Give the extent of all Plasmodium falciparum-infected red blood cells.
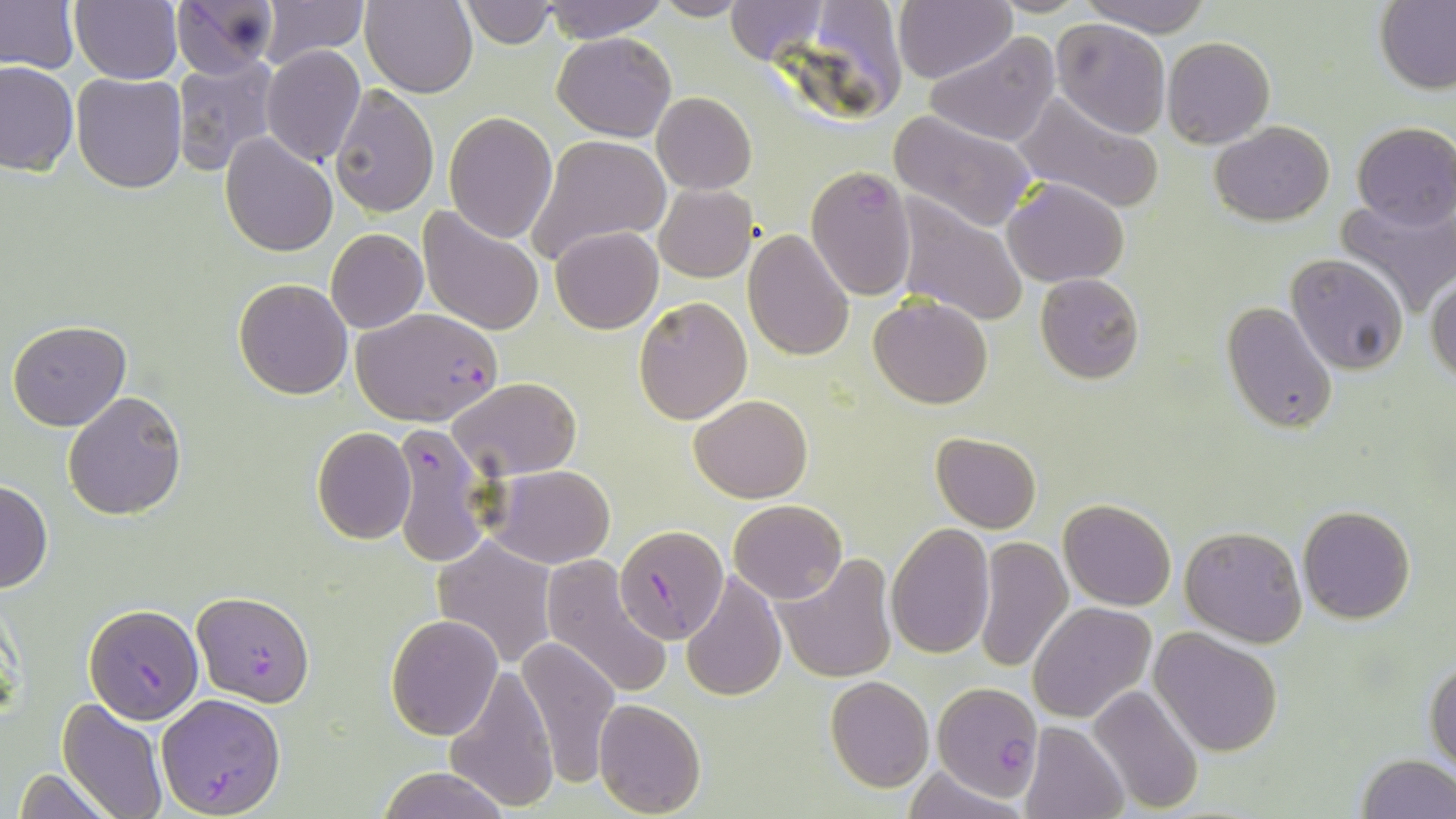

Approximate bounding boxes as (x1,y1)-(x2,y2) corner pairs in pixels.
Plasmodium falciparum-infected red blood cells: (806,166)-(916,300), (352,309)-(504,426), (387,422)-(495,565), (613,523)-(726,643), (192,592)-(315,706), (83,604)-(205,723), (933,683)-(1042,801), (155,693)-(286,817).

Uninfected red blood cell locations: (0,0)-(80,74), (173,0)-(276,78), (360,0)-(477,96), (460,0)-(558,48), (538,0)-(671,44), (651,0)-(753,21), (724,0)-(830,65), (893,0)-(1013,85), (1081,0)-(1213,37), (69,1)-(183,84), (257,1)-(367,66), (1376,2)-(1456,94), (1052,18)-(1170,138), (552,30)-(676,141), (922,31)-(1061,147), (1162,37)-(1275,149), (261,44)-(366,167), (171,55)-(279,175), (1,60)-(78,175), (188,66)-(308,225), (71,73)-(189,193), (330,85)-(438,218), (1011,87)-(1164,214), (652,92)-(756,193), (443,112)-(558,243), (889,112)-(1037,233), (1209,120)-(1336,226), (1351,120)-(1456,230), (220,133)-(338,258), (525,133)-(671,267), (1003,178)-(1129,288), (654,184)-(756,282), (892,193)-(1030,328), (1333,193)-(1456,318), (418,209)-(544,335), (550,226)-(663,334), (742,227)-(855,361), (326,229)-(427,333), (1284,254)-(1408,374), (1035,273)-(1144,384), (1427,275)-(1456,385), (234,278)-(352,399), (634,295)-(752,425), (868,295)-(993,409), (1220,301)-(1339,433), (7,321)-(131,430), (449,376)-(582,478), (63,389)-(186,520), (690,393)-(813,504), (311,427)-(415,544), (932,432)-(1042,532), (489,465)-(616,568), (0,479)-(52,595), (1060,498)-(1175,610), (729,499)-(846,603), (1297,505)-(1416,623), (886,522)-(994,658), (1180,526)-(1308,647), (431,535)-(558,669), (973,536)-(1073,674), (777,554)-(897,683), (540,555)-(674,701), (682,570)-(786,702), (1027,602)-(1158,723), (386,615)-(502,739), (1151,631)-(1282,756), (516,635)-(620,787), (1425,656)-(1456,773), (444,663)-(561,814), (825,675)-(934,791), (1085,683)-(1203,814), (593,697)-(707,818), (59,699)-(169,819), (1019,720)-(1129,819), (1354,752)-(1456,819), (900,764)-(1028,819), (375,766)-(509,819), (10,769)-(114,819). Slide-level diagnosis: Plasmodium falciparum. Light microscopy. Thin blood film. Captured at 1000x magnification. Image is 1456×819 pixels. Single field of view. May-Grünwald-Giemsa stain.